Locate and identify every blood parasite.
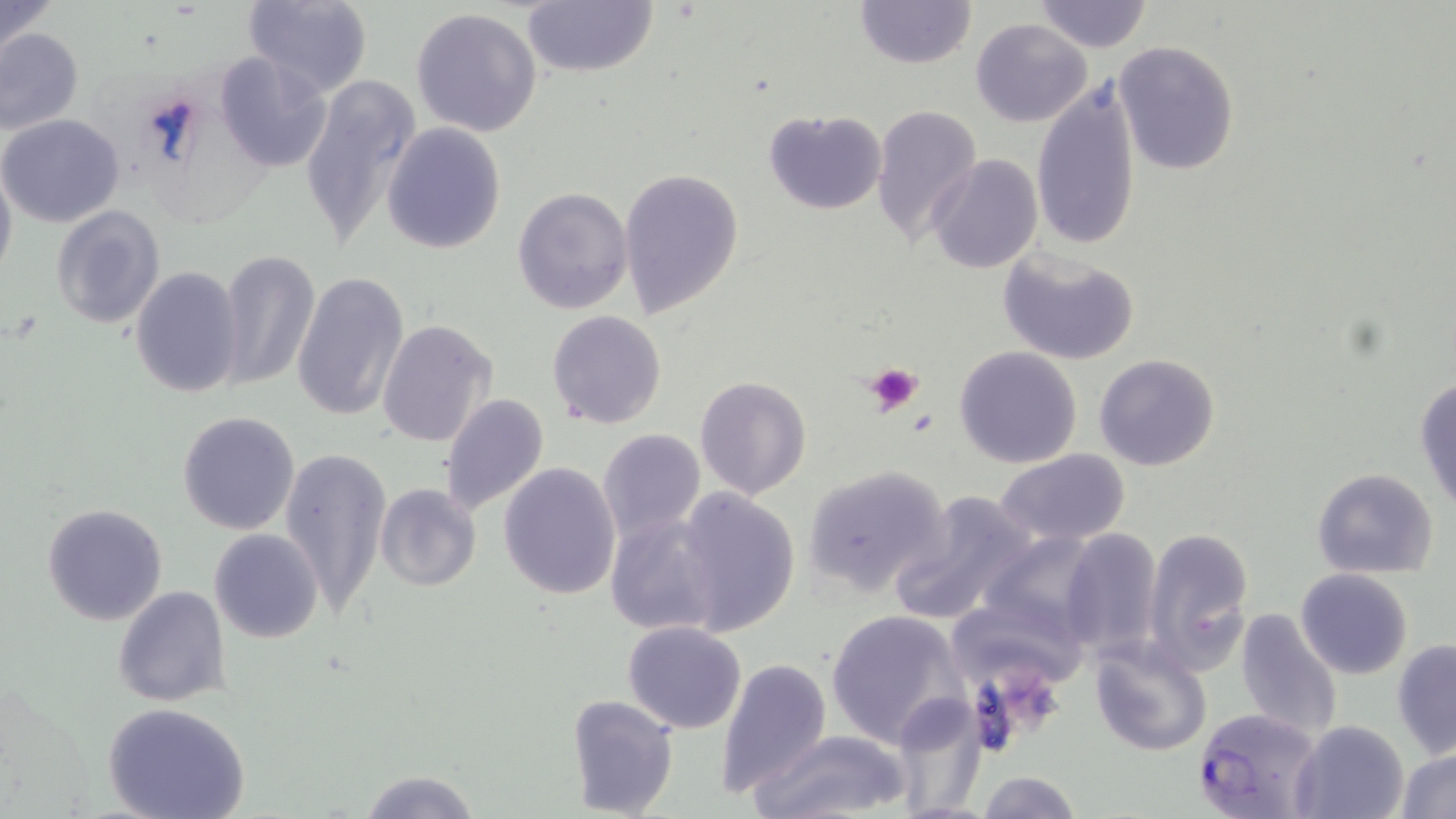

Approximate bounding boxes as (x1,y1)-(x2,y2) corner pairs in pixels.
Plasmodium falciparum-infected red blood cells: (1192,708)-(1324,817).
No Plasmodium ovale, Plasmodium malariae, Plasmodium vivax, Babesia divergens, or Trypanosoma brucei observed.

Platelet locations: (864,361)-(925,416). Uninfected red blood cell locations: (0,0)-(59,54), (243,0)-(373,98), (520,0)-(658,80), (854,0)-(977,71), (1033,1)-(1152,51), (410,7)-(543,139), (972,17)-(1093,126), (0,29)-(84,135), (1115,41)-(1239,174), (215,51)-(334,172), (298,75)-(422,255), (1031,76)-(1140,253), (869,104)-(982,246), (762,108)-(887,215), (0,113)-(124,226), (382,122)-(507,254), (928,155)-(1042,274), (0,160)-(17,287), (619,169)-(744,319), (513,188)-(634,313), (50,205)-(166,330), (996,248)-(1140,366), (217,249)-(320,391), (131,267)-(244,398), (292,270)-(409,423), (548,311)-(666,429), (376,319)-(497,448), (953,344)-(1083,469), (1094,354)-(1221,472), (1414,375)-(1456,511), (694,376)-(812,499), (438,394)-(551,518), (177,410)-(302,535), (598,429)-(704,542), (280,447)-(390,616), (995,450)-(1133,545), (499,461)-(621,599), (802,463)-(954,598), (1312,468)-(1439,578), (374,483)-(481,592), (675,487)-(800,634), (890,490)-(1043,626), (42,502)-(167,626), (605,510)-(724,637), (1142,525)-(1254,676), (1056,527)-(1164,659), (209,529)-(323,642), (1297,569)-(1413,679), (114,585)-(231,708), (944,606)-(1086,690), (1233,606)-(1343,742), (825,609)-(968,749), (623,621)-(747,733), (583,634)-(721,781), (1089,635)-(1212,755), (1392,638)-(1456,759), (716,655)-(832,797), (889,690)-(990,815), (566,692)-(679,817), (102,702)-(250,819), (1290,718)-(1410,819), (753,730)-(908,819), (1396,747)-(1456,819), (356,770)-(484,819), (976,771)-(1086,818). Slide-level diagnosis: Plasmodium falciparum. Image is 1456×819 pixels. Captured at 1000x magnification. Single field of view. May-Grünwald-Giemsa-stained preparation. Thin blood film. Optical microscopy.